Report the malaria status of this cell.
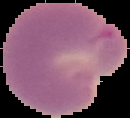
Parasitized.

Summary:
  - Image size: 130×118 pixels
  - Preparation: thin blood film
  - Image type: cell region segmented out of the field of view; surrounding area masked to black